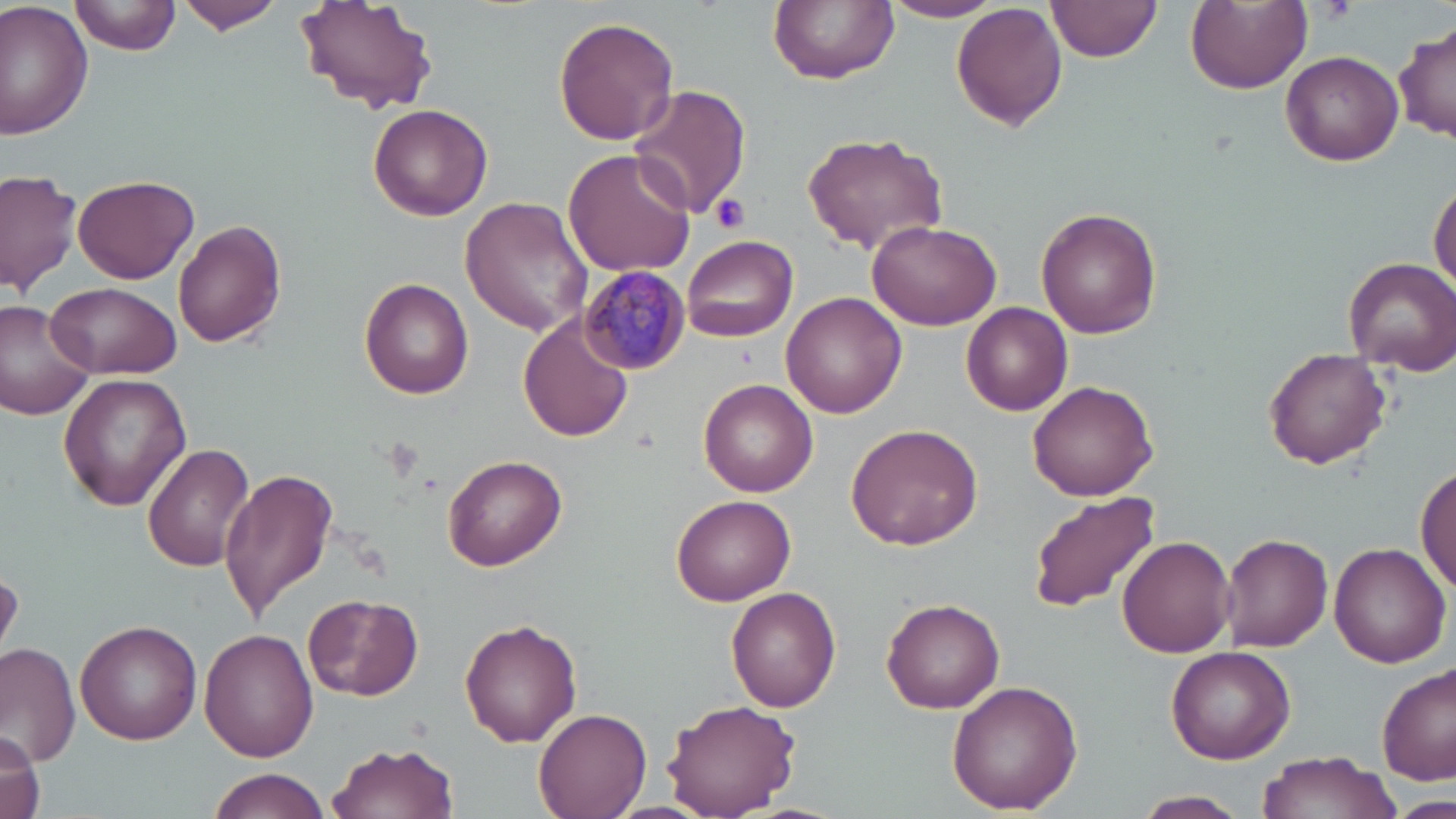
slide-level diagnosis = Plasmodium malariae
stain = May-Grünwald-Giemsa
modality = optical microscopy
Plasmodium malariae-infected red blood cell locations = approximate bounding boxes as [x1, y1, x2, y2] in pixels: [579, 266, 689, 373]
preparation = thin blood smear
image size = 1456×819 pixels
uninfected red blood cell locations = approximate bounding boxes as [x1, y1, x2, y2] in pixels: [73, 0, 179, 57], [179, 0, 287, 35], [295, 0, 438, 115], [768, 0, 899, 86], [880, 0, 1008, 23], [1184, 0, 1310, 93], [0, 1, 96, 141], [1045, 1, 1161, 65], [952, 4, 1069, 133], [555, 17, 679, 145], [1395, 22, 1455, 143], [1281, 50, 1403, 166], [628, 84, 751, 219], [368, 103, 494, 220], [799, 130, 952, 258], [562, 148, 698, 280], [0, 168, 83, 295], [73, 173, 200, 283], [1429, 181, 1456, 294], [459, 196, 591, 336], [1036, 209, 1162, 338], [865, 218, 1001, 329], [171, 220, 285, 349], [680, 234, 799, 344], [1342, 255, 1456, 372], [359, 277, 475, 399], [45, 280, 184, 380], [780, 292, 907, 419], [0, 300, 97, 422], [961, 302, 1073, 417], [519, 315, 634, 443], [1262, 350, 1392, 470], [58, 373, 190, 511], [698, 378, 819, 496], [1026, 380, 1159, 501], [847, 422, 985, 549], [145, 443, 255, 573], [443, 454, 566, 569], [1416, 461, 1455, 598], [220, 468, 337, 623], [1027, 493, 1159, 614], [672, 494, 797, 605], [1220, 533, 1334, 651], [1117, 536, 1235, 658], [1328, 540, 1451, 668], [726, 587, 841, 712], [302, 594, 424, 700], [882, 599, 1003, 714], [75, 620, 202, 745], [458, 620, 582, 747], [201, 629, 319, 762], [0, 640, 80, 770], [1166, 646, 1296, 764], [1376, 662, 1455, 785], [946, 678, 1084, 814], [662, 698, 801, 817], [533, 707, 651, 818], [1, 726, 45, 819], [327, 739, 459, 819], [1257, 751, 1398, 817], [206, 768, 329, 819], [1137, 791, 1250, 816]
magnification = 1000x
platelet locations = approximate bounding boxes as [x1, y1, x2, y2] in pixels: [1316, 0, 1358, 25], [711, 193, 752, 234]
field of view = one of a larger specimen